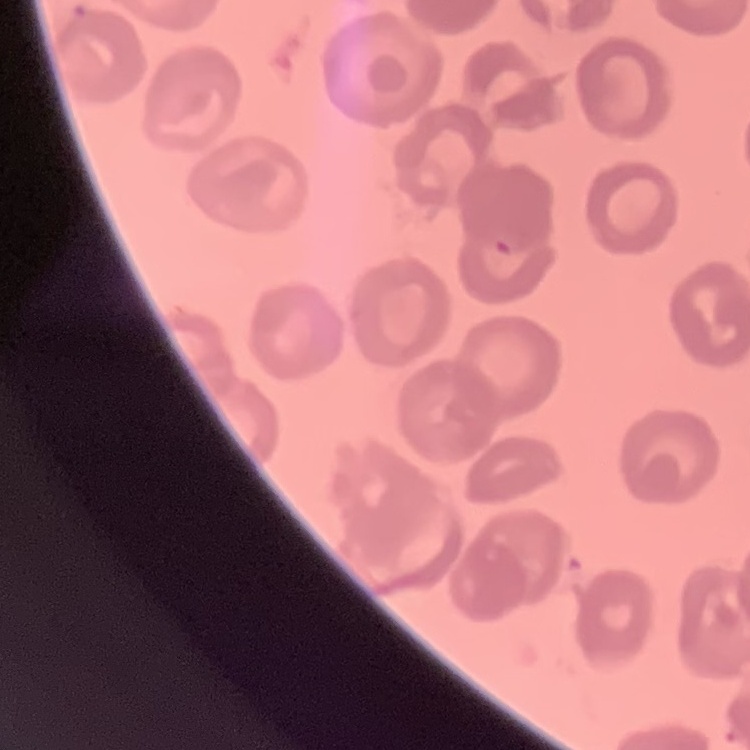
Summary:
  - Red blood cell morphology: no rouleaux formation
  - Preparation: thin blood film
  - Stain: Field's or Giemsa
  - Image type: one tile cut from a larger photomicrograph